Assess the morphology of the red blood cells.
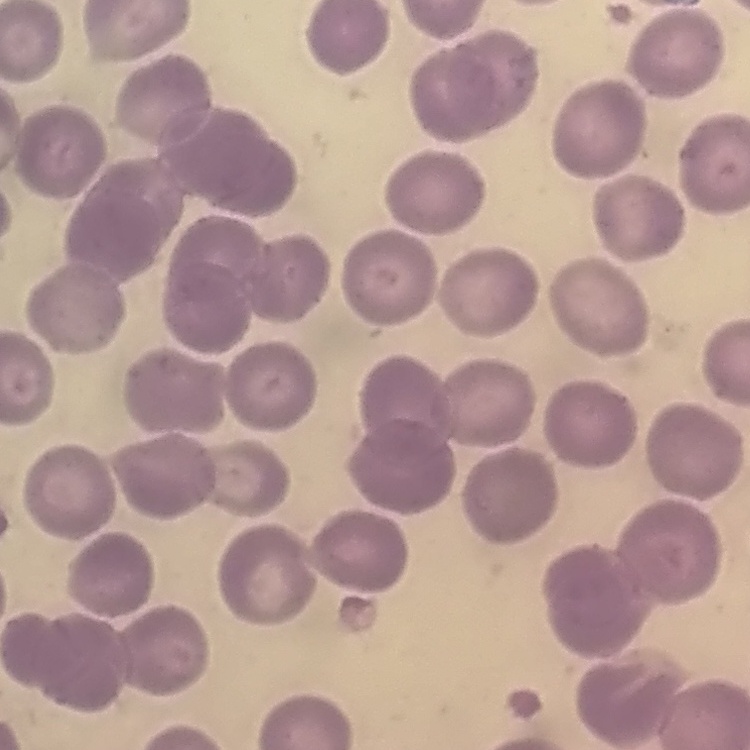

No rouleaux formation.

Square crop of a larger photomicrograph. Thin blood film. Field's or Giemsa stain.